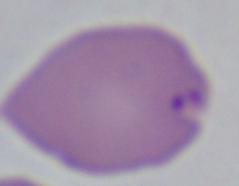 Micrograph. A Babesia parasite is shown. Captured at 1000x magnification.